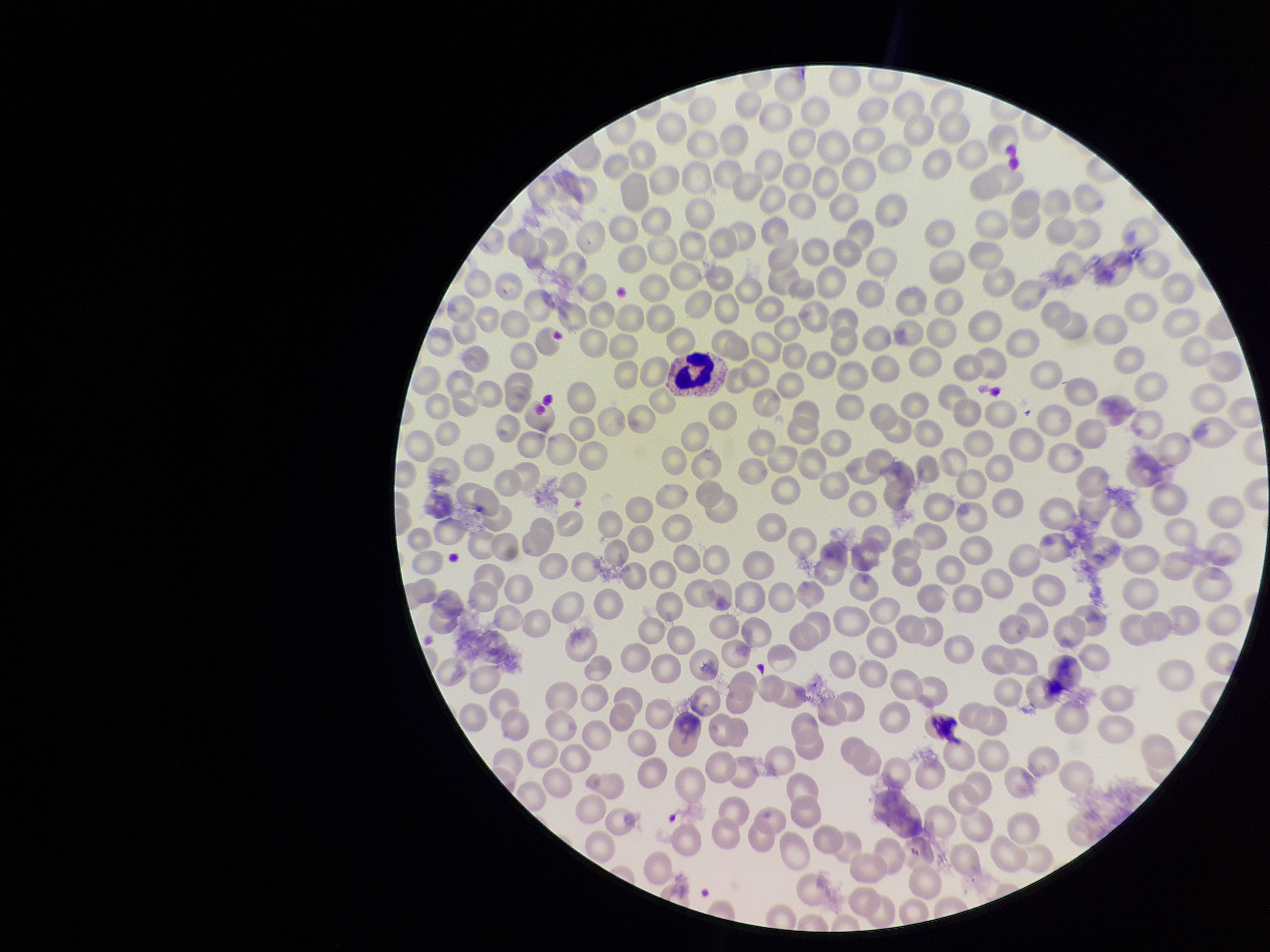

parasitized red blood cells = none identified
stain = Giemsa
species reported for this patient = Plasmodium vivax
field of view = one from this slide
preparation = thin smear
patient malaria status = positive
capture = smartphone photograph through the microscope eyepiece
image size = 1270×952 pixels
red blood cell count = 313
parasitized red blood cell count = 0